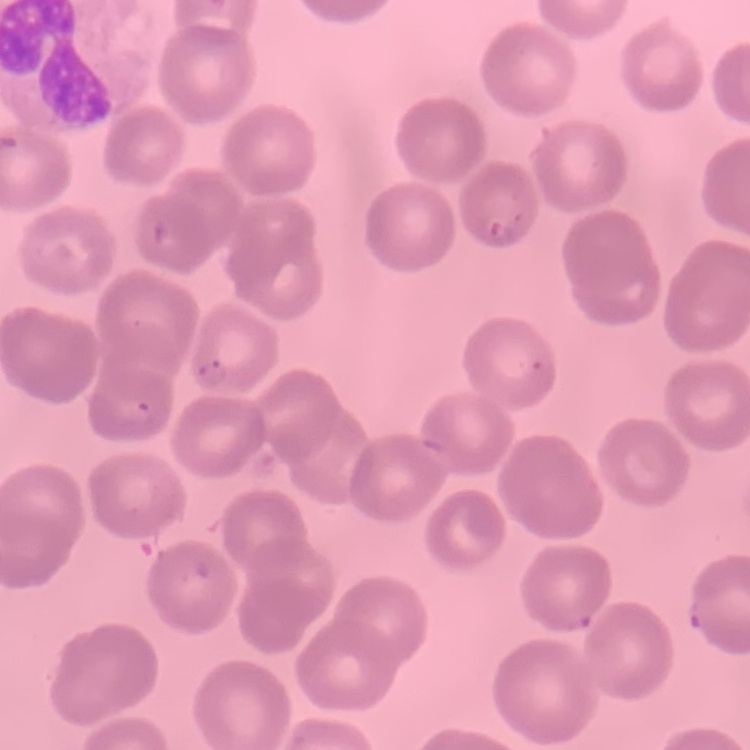
erythrocyte morphology = no rouleaux formation
image type = one tile cut from a larger photomicrograph
preparation = thin peripheral smear
stain = Field's or Giemsa